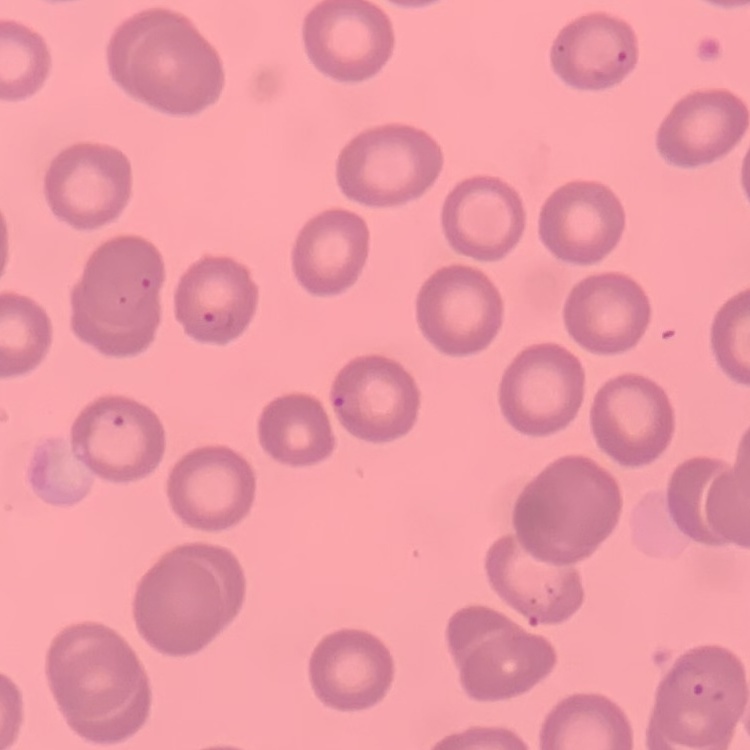

red blood cell morphology = no rouleaux formation
stain = Field's or Giemsa
image type = one tile cut from a larger photomicrograph
preparation = thin peripheral smear